Comment on the morphology of the erythrocytes.
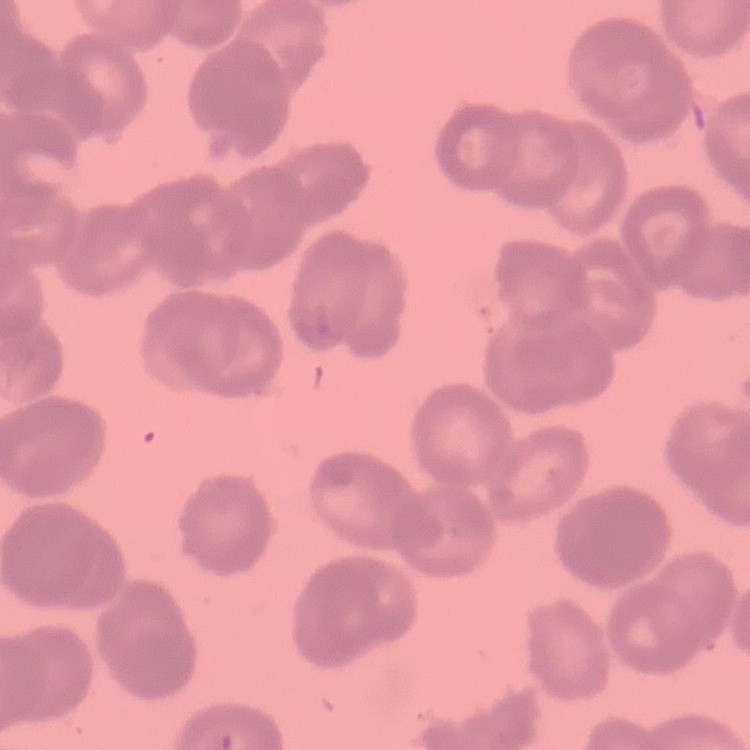
Rouleaux formation.

Summary:
  - Preparation: thin blood smear
  - Stain: Field's or Giemsa
  - Image type: one tile cut from a larger photomicrograph